Point out each malaria parasite.
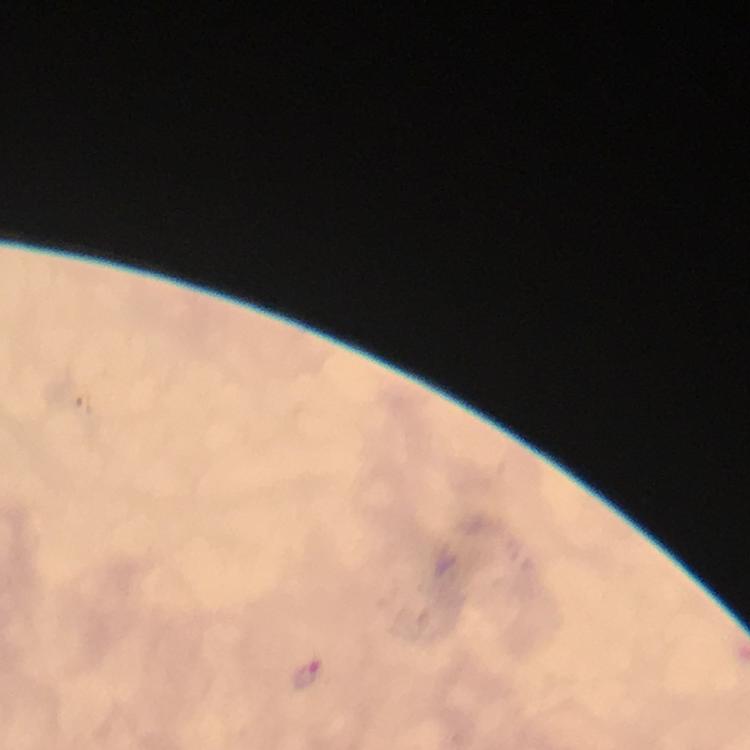

Approximate centers as {x, y} in pixels.
Malaria parasites: {306, 676}.

Summary:
  - Immersion oil: used
  - Stain: Giemsa
  - Magnification: 100x
  - Preparation: thick blood smear
  - Capture: smartphone camera through the microscope
  - Image size: 750×750 pixels
  - Context: from a malaria diagnostic workup
  - Cropped from: a single field of view